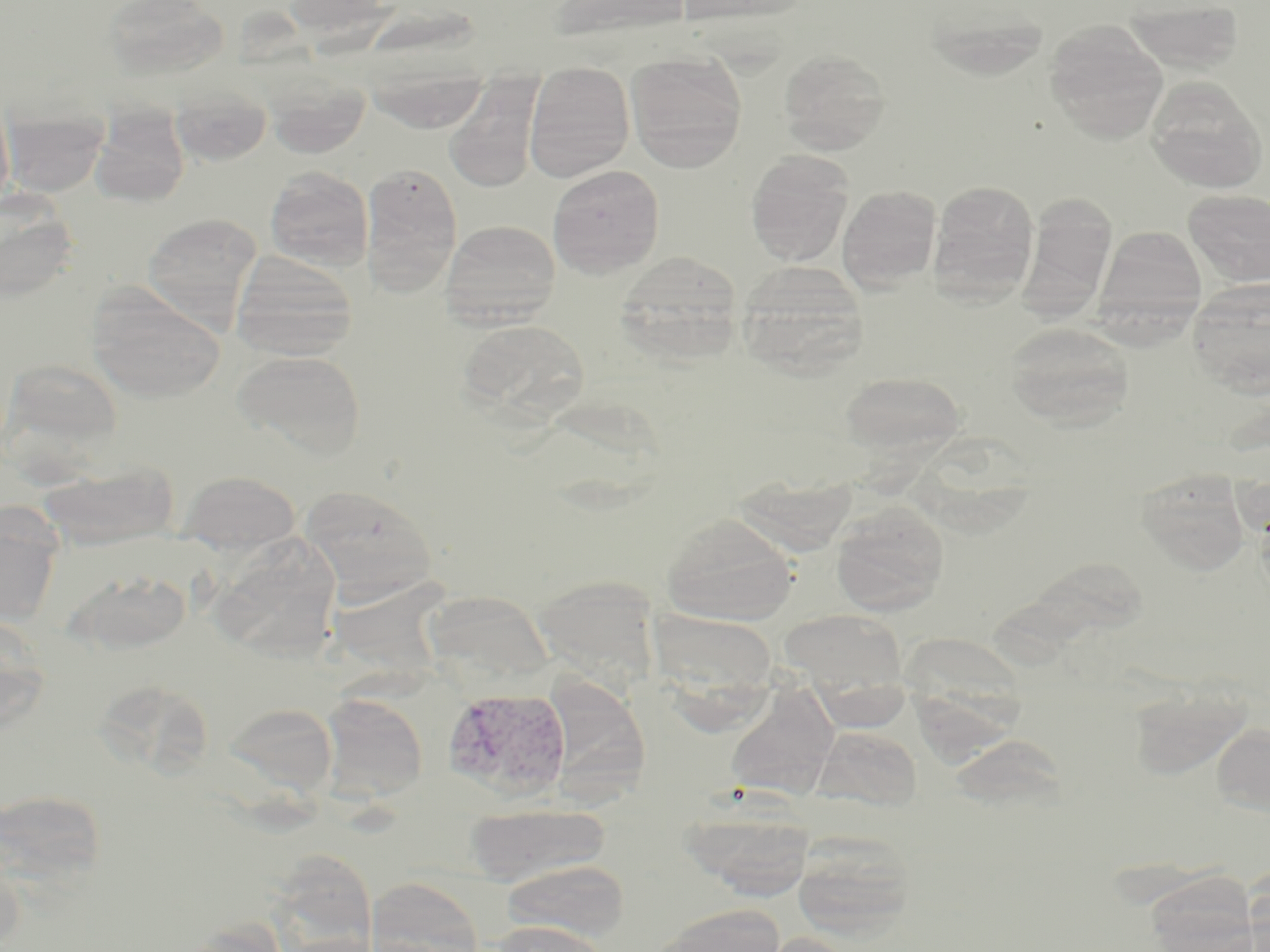

Summary:
  - Coordinate format: approximate bounding boxes as (x1, y1, x2, y2) in pixels
  - Plasmodium vivax-infected red blood cell locations: (442, 687, 572, 801)
  - Uninfected red blood cell locations: (102, 0, 229, 84), (281, 0, 390, 36), (548, 0, 692, 43), (674, 0, 812, 26), (1120, 1, 1245, 76), (1044, 22, 1168, 143), (778, 48, 891, 154), (625, 51, 748, 172), (362, 58, 492, 132), (524, 62, 635, 182), (267, 73, 370, 158), (444, 79, 543, 192), (1146, 79, 1268, 193), (171, 83, 272, 167), (0, 85, 15, 214), (3, 108, 108, 198), (89, 108, 190, 207), (746, 150, 854, 266), (359, 163, 463, 295), (548, 165, 665, 277), (265, 166, 373, 271), (930, 181, 1039, 299), (837, 186, 941, 292), (0, 189, 80, 300), (1183, 190, 1270, 287), (142, 212, 262, 328), (440, 219, 561, 327), (1094, 224, 1208, 327), (614, 250, 743, 364), (230, 252, 359, 361), (736, 261, 868, 375), (1188, 283, 1270, 396), (85, 286, 227, 402), (1004, 321, 1136, 430), (456, 323, 588, 430), (232, 349, 367, 460), (838, 371, 967, 459), (38, 461, 181, 550), (178, 469, 303, 555), (1135, 470, 1251, 575), (733, 472, 859, 555), (300, 483, 438, 601), (830, 501, 949, 616), (0, 507, 63, 627), (661, 512, 798, 625), (208, 538, 342, 662), (72, 570, 192, 655), (531, 574, 661, 683), (420, 589, 556, 690), (778, 609, 908, 705), (0, 616, 50, 734), (724, 682, 839, 799), (1129, 682, 1253, 780), (319, 694, 428, 802), (223, 703, 338, 796), (1210, 722, 1270, 817), (814, 726, 922, 810), (0, 787, 108, 896), (464, 804, 611, 887), (682, 806, 815, 897), (792, 832, 915, 938), (263, 849, 379, 951), (500, 859, 630, 942), (365, 876, 487, 952), (652, 904, 785, 952), (174, 916, 289, 952), (488, 919, 611, 952), (750, 932, 863, 952)
  - Slide-level diagnosis: Plasmodium vivax
  - Field of view: one of a larger specimen
  - Magnification: 1000x
  - Preparation: thin blood smear
  - Modality: optical microscopy
  - Image size: 1270×952 pixels
  - Stain: May-Grünwald-Giemsa